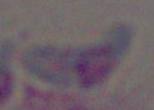
magnification = 1000x
identification = Toxoplasma gondii
modality = micrograph